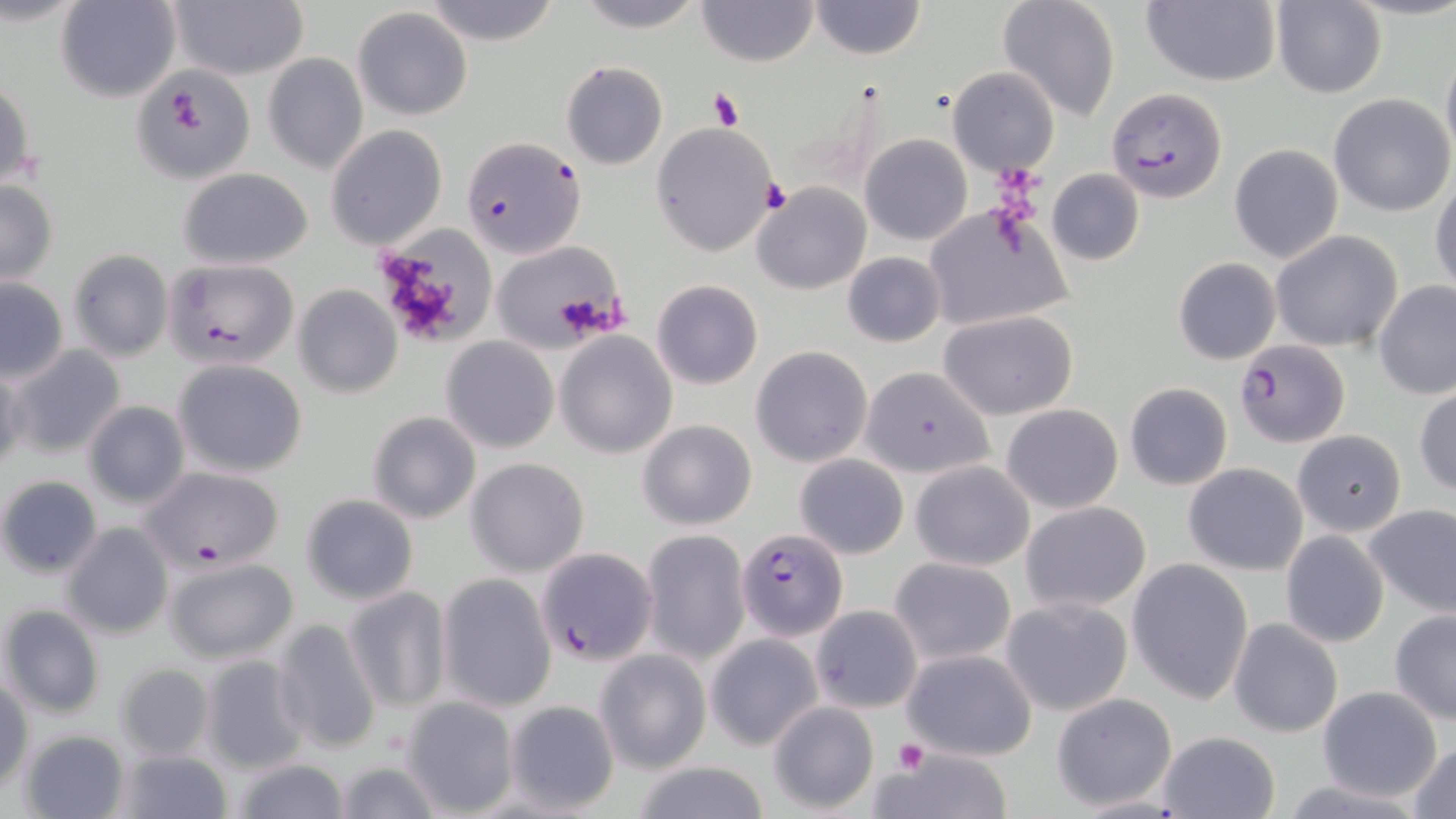

slide_level_diagnosis: Plasmodium falciparum
stain: May-Grünwald-Giemsa
plasmodium_falciparum_infected_red_blood_cell_locations: 'approximate bounding boxes as (x1, y1, x2, y2) in pixels: (1106, 87, 1228, 204), (463, 136, 585, 260), (163, 259, 301, 371), (1234, 340, 1349, 449), (135, 465, 286, 575), (737, 526, 848, 639), (535, 546, 659, 666)'
preparation: thin blood film
field_of_view: one of a larger specimen
magnification: 1000x
uninfected_red_blood_cell_locations: 'approximate bounding boxes as (x1, y1, x2, y2) in pixels: (57, 0, 180, 102), (421, 0, 560, 45), (572, 0, 707, 32), (809, 0, 926, 60), (997, 0, 1122, 122), (1141, 0, 1282, 87), (167, 1, 309, 82), (696, 1, 819, 67), (1270, 2, 1386, 97), (352, 7, 472, 119), (263, 54, 368, 174), (561, 62, 667, 170), (947, 68, 1058, 175), (131, 69, 252, 180), (0, 75, 35, 193), (1329, 93, 1454, 216), (651, 123, 781, 256), (326, 125, 447, 250), (860, 133, 972, 245), (1228, 143, 1343, 263), (176, 168, 315, 269), (1046, 168, 1144, 266), (1430, 173, 1456, 297), (0, 181, 59, 283), (751, 182, 870, 295), (922, 208, 1070, 334), (375, 226, 494, 347), (1269, 230, 1402, 353), (487, 243, 628, 353), (67, 249, 173, 362), (842, 252, 945, 347), (1173, 257, 1281, 365), (0, 277, 69, 382), (651, 280, 762, 389), (1373, 280, 1455, 401), (297, 285, 407, 398), (940, 311, 1077, 421), (554, 332, 678, 459), (441, 337, 560, 454), (9, 344, 127, 458), (750, 345, 872, 467), (174, 359, 308, 477), (861, 365, 996, 481), (0, 366, 24, 479), (1125, 382, 1232, 490), (1415, 387, 1456, 496), (81, 400, 190, 509), (1001, 403, 1123, 513), (367, 412, 482, 525), (636, 418, 758, 531), (1292, 429, 1406, 537), (795, 454, 909, 559), (466, 458, 590, 576), (910, 461, 1035, 570), (1183, 463, 1309, 574), (1, 475, 102, 578), (299, 492, 420, 606), (1019, 502, 1152, 612), (1364, 503, 1456, 620), (62, 522, 174, 639), (640, 529, 750, 665), (1279, 529, 1389, 648), (889, 556, 1017, 666), (1126, 557, 1254, 705), (160, 560, 297, 667), (436, 574, 557, 713), (342, 586, 452, 714), (1000, 596, 1133, 717), (1, 603, 105, 720), (810, 606, 923, 713), (1389, 610, 1456, 725), (270, 617, 384, 756), (1227, 617, 1343, 739), (705, 633, 823, 750), (593, 647, 713, 774), (901, 648, 1037, 760), (198, 654, 309, 773), (114, 663, 215, 762), (0, 677, 32, 792), (1315, 685, 1443, 802), (1051, 692, 1178, 811), (400, 694, 519, 814), (506, 699, 621, 814), (767, 701, 880, 814), (20, 730, 131, 819), (1156, 730, 1280, 818), (1408, 740, 1456, 818), (869, 746, 1012, 819), (114, 749, 231, 818), (229, 757, 353, 819), (328, 758, 443, 819), (625, 762, 775, 819)'
modality: light microscopy
image_size: 1456×819 pixels
platelet_locations: 'approximate bounding boxes as (x1, y1, x2, y2) in pixels: (163, 76, 218, 136), (708, 88, 743, 131), (763, 178, 791, 213), (893, 740, 929, 777)'